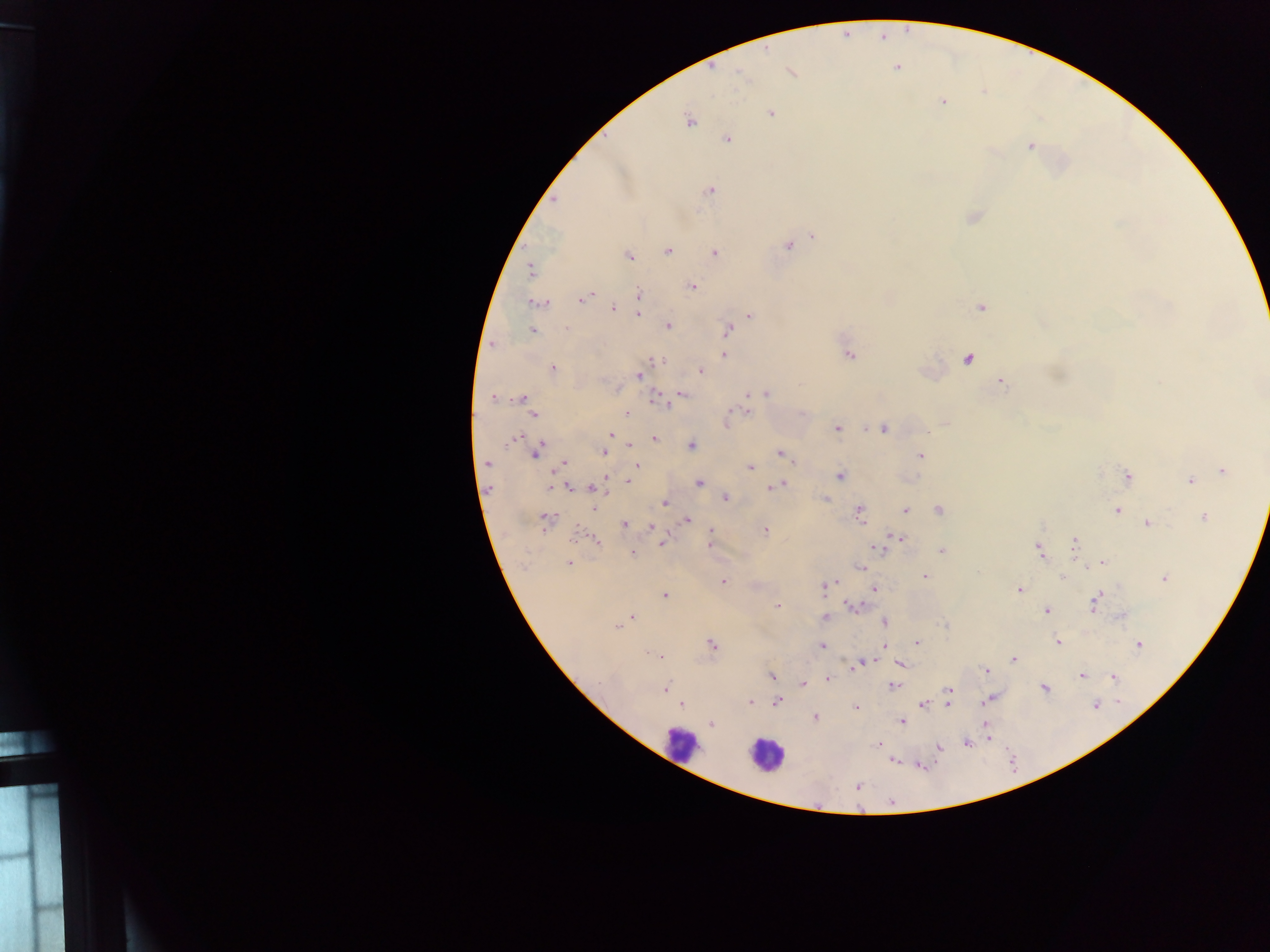
Plasmodium parasite locations = approximate centers as {x, y} in pixels: {846, 34}, {882, 36}, {897, 67}, {711, 68}, {791, 72}, {942, 101}, {771, 113}, {689, 120}, {726, 138}, {1030, 146}, {709, 189}, {553, 198}, {973, 217}, {814, 235}, {788, 245}, {667, 251}, {714, 252}, {628, 256}, {530, 268}, {692, 286}, {637, 294}, {584, 298}, {537, 303}, {613, 307}, {979, 307}, {637, 314}, {750, 315}, {667, 326}, {566, 328}, {727, 329}, {531, 330}, {492, 343}, {725, 344}, {848, 353}, {724, 354}, {967, 358}, {655, 359}, {552, 369}, {700, 370}, {638, 375}, {999, 381}, {680, 392}, {749, 393}, {760, 393}, {766, 393}, {493, 397}, {655, 397}, {521, 398}, {746, 409}, {626, 413}, {534, 414}, {728, 420}, {945, 423}, {836, 428}, {884, 428}, {611, 433}, {513, 437}, {653, 439}, {609, 441}, {631, 445}, {691, 445}, {538, 450}, {604, 451}, {781, 453}, {920, 455}, {486, 463}, {564, 463}, {637, 465}, {749, 467}, {559, 468}, {1222, 471}, {840, 475}, {606, 477}, {1128, 477}, {629, 480}, {1190, 481}, {699, 483}, {779, 483}, {558, 485}, {551, 486}, {772, 486}, {565, 487}, {592, 488}, {486, 490}, {725, 497}, {825, 498}, {664, 502}, {593, 506}, {859, 510}, {905, 510}, {938, 510}, {1117, 510}, {1203, 517}, {685, 519}, {546, 521}, {1147, 523}, {623, 524}, {651, 526}, {764, 529}, {710, 531}, {577, 535}, {898, 537}, {595, 539}, {1075, 541}, {662, 542}, {709, 544}, {875, 548}, {1039, 549}, {940, 550}, {632, 553}, {1101, 562}, {569, 563}, {860, 567}, {924, 576}, {1063, 576}, {1164, 578}, {723, 581}, {836, 582}, {826, 584}, {874, 588}, {1019, 589}, {665, 595}, {1095, 602}, {852, 605}, {778, 606}, {1047, 610}, {1122, 615}, {823, 616}, {630, 617}, {884, 621}, {617, 626}, {917, 642}, {1057, 642}, {710, 644}, {821, 645}, {1137, 645}, {884, 646}, {651, 654}, {658, 656}, {1012, 660}, {861, 663}, {900, 663}, {853, 666}, {985, 671}, {771, 676}, {1081, 676}, {1114, 677}, {828, 678}, {803, 683}, {893, 685}, {1043, 687}, {665, 689}, {948, 689}, {990, 698}, {777, 701}, {749, 702}, {947, 703}, {680, 704}, {923, 705}, {855, 708}, {815, 717}, {901, 721}, {711, 724}, {985, 725}, {986, 733}, {986, 739}, {965, 742}, {878, 744}, {939, 748}, {892, 760}, {917, 765}, {857, 785}
field of view = single
preparation = thick blood film
capture = mobile-phone photograph through a microscope
leukocyte locations = approximate centers as {x, y} in pixels: {681, 742}, {766, 755}
image size = 1270×952 pixels
country = Ghana